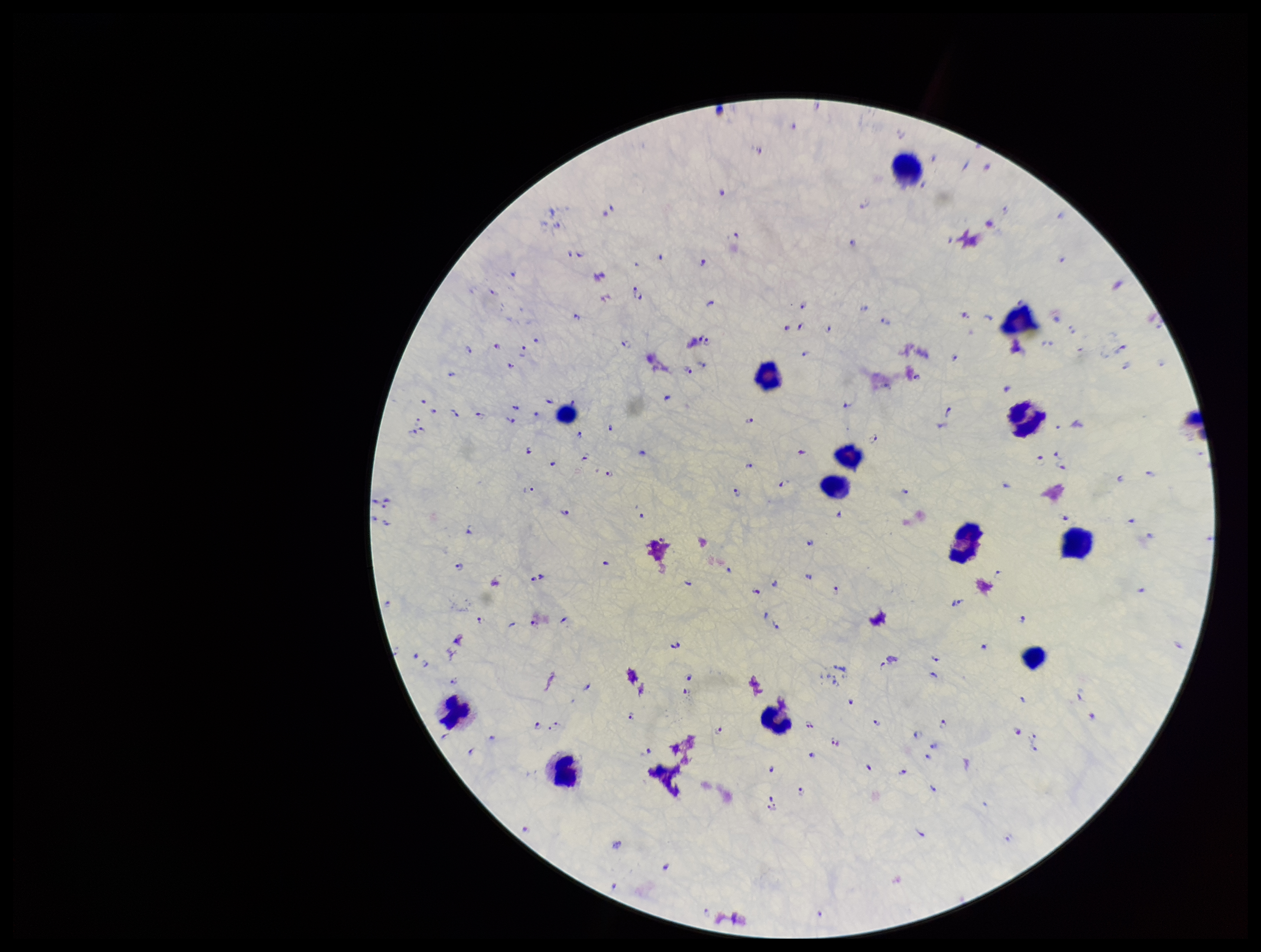
{
  "parasite_count": 170,
  "leukocyte_count": 14,
  "stain": "Giemsa",
  "preparation": "thick blood smear",
  "field_of_view": "single",
  "plasmodium_parasites": "seen",
  "capture": "smartphone photograph through the microscope eyepiece",
  "image_size": "1261×952 pixels",
  "species_reported_for_this_patient": "Plasmodium falciparum",
  "patient_malaria_status": "positive"
}